Give the position of each Plasmodium falciparum parasite with its life-cycle stage, each leukocyte, and any debris.
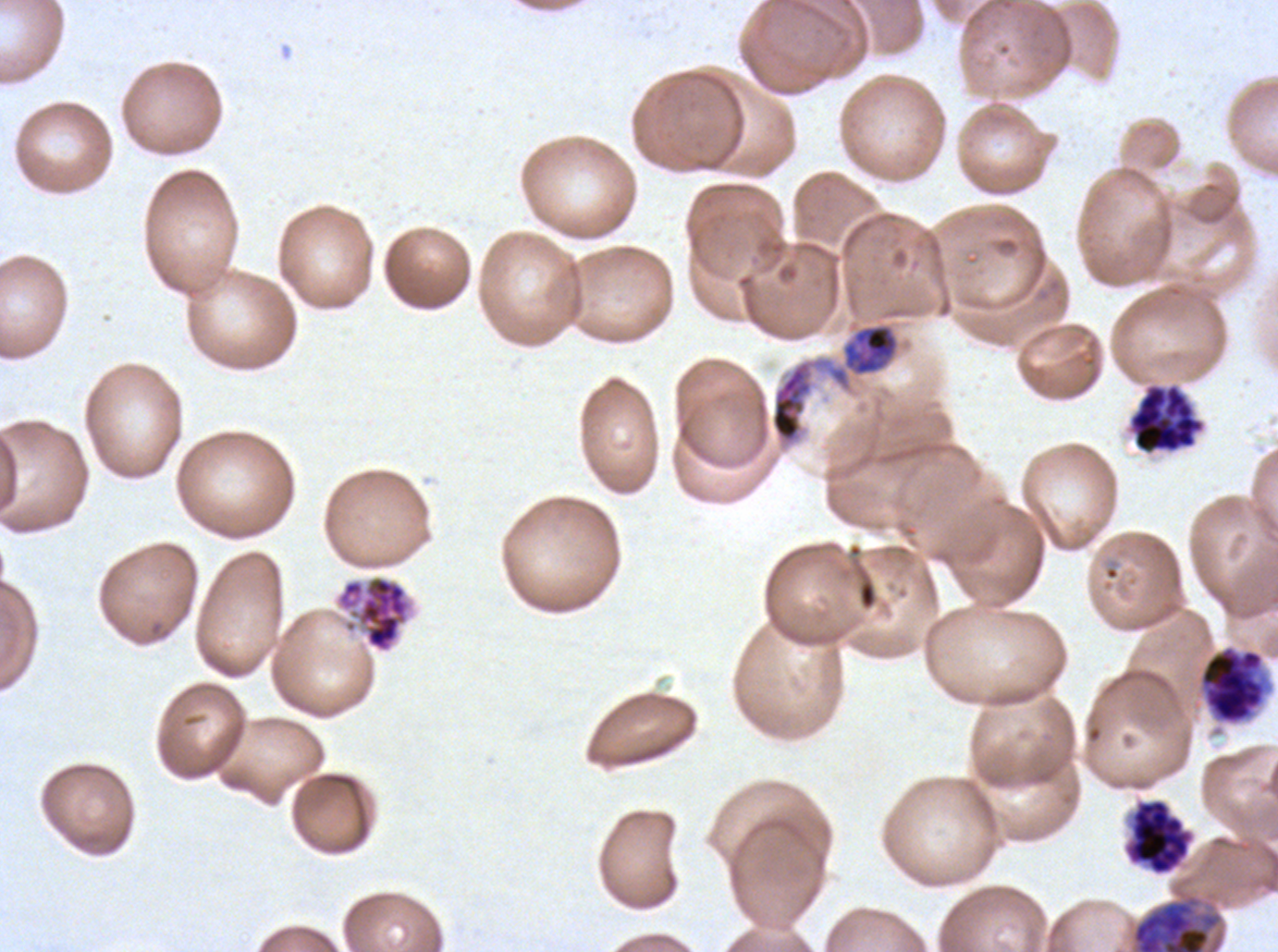
Approximate bounding boxes as {x1, y1, x2, y2} in pixels.
Mid trophozoites: {842, 324, 899, 376}.
Early schizonts: {769, 360, 814, 445}, {1197, 643, 1274, 727}.
Late schizonts: {1128, 384, 1205, 455}, {333, 573, 416, 654}.
Segmenters: {1124, 798, 1194, 876}.
No rings, late-ring/early-trophozoite forms, late trophozoites, gametocytes, leukocytes, or debris observed.

{
  "preparation": "thin blood film",
  "stain": "Giemsa",
  "field_of_view": "one sub-image of a larger composite",
  "specimen": "ex-vivo Plasmodium falciparum culture from a patient in The Gambia, grown for 24 to 48 hours",
  "life_cycle_stages_observed": "mid trophozoite, early schizont, late schizont, segmenter",
  "image_size": "1278×952 pixels"
}